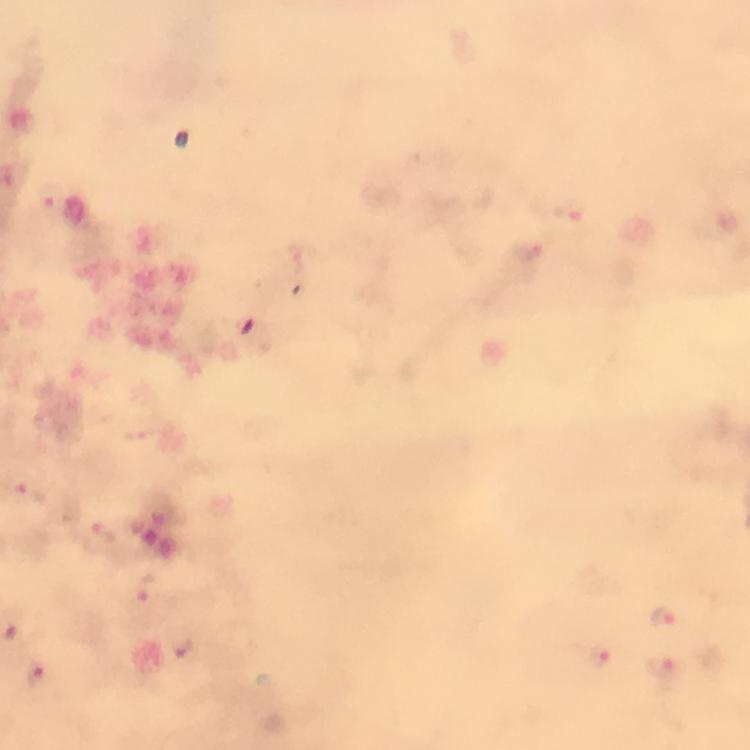
Approximate centers as (x, y) in pixels.
Summary:
  - Plasmodium parasite locations: (50, 197), (571, 210), (526, 249), (139, 435), (32, 490), (105, 534), (146, 588), (662, 615), (182, 644), (600, 657), (665, 668), (35, 675)
  - Context: from a diagnostic examination for malaria
  - Stain: Giemsa
  - Image size: 750×750 pixels
  - Cropped from: one field of view
  - Capture: smartphone camera through the microscope
  - Preparation: thick smear
  - Immersion oil: applied
  - Magnification: 100x